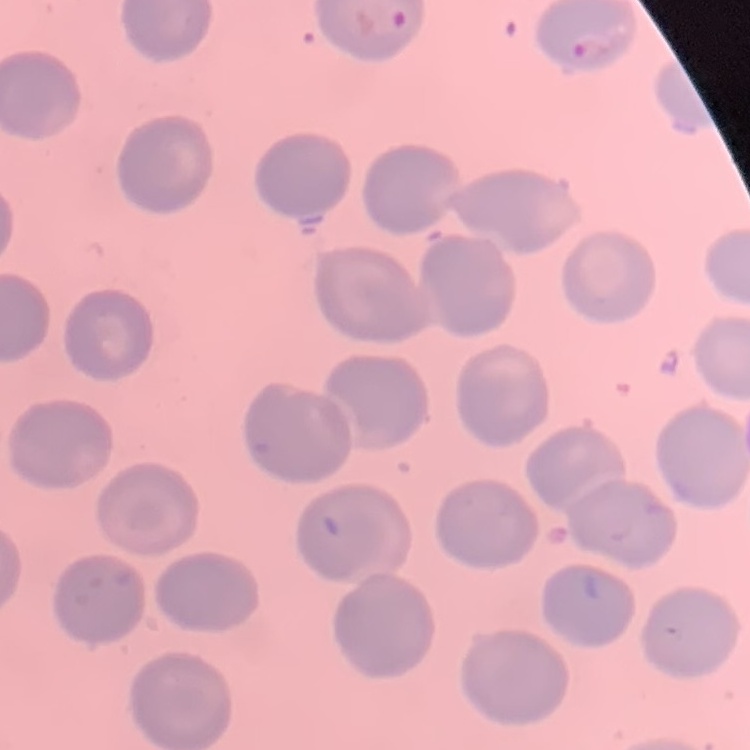

red blood cell morphology = no rouleaux formation
image type = one tile cut from a larger photomicrograph
preparation = thin blood smear
stain = Field's or Giemsa